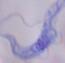 A trypanosome is seen. Micrograph. 1000x magnification.